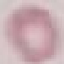

malaria status = uninfected
stain = Giemsa
capture = smartphone camera at the microscope eyepiece
image type = cell patch, automatically extracted from a larger field of view and resized to 64 × 64 pixels
preparation = thin blood smear